Classify this cell by malaria status.
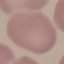
Uninfected.

Photographed with a smartphone camera at the microscope eyepiece. Thin blood smear. Giemsa stain. Automatically extracted cell patch, resized to 64 × 64 pixels.